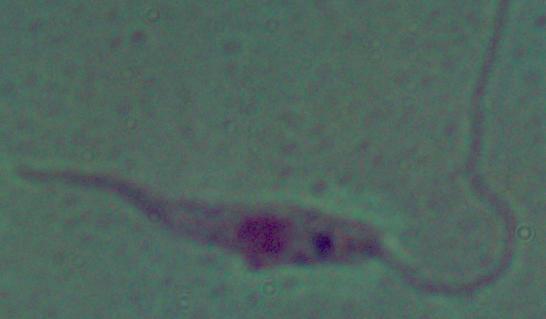

Summary:
  - Magnification: 1000x
  - Modality: micrograph
  - Identification: Leishmania